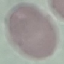
result = no malaria parasites detected
image type = automatically extracted cell patch, resized to 64 × 64 pixels
stain = Giemsa
preparation = thin blood film
capture = smartphone through the microscope eyepiece